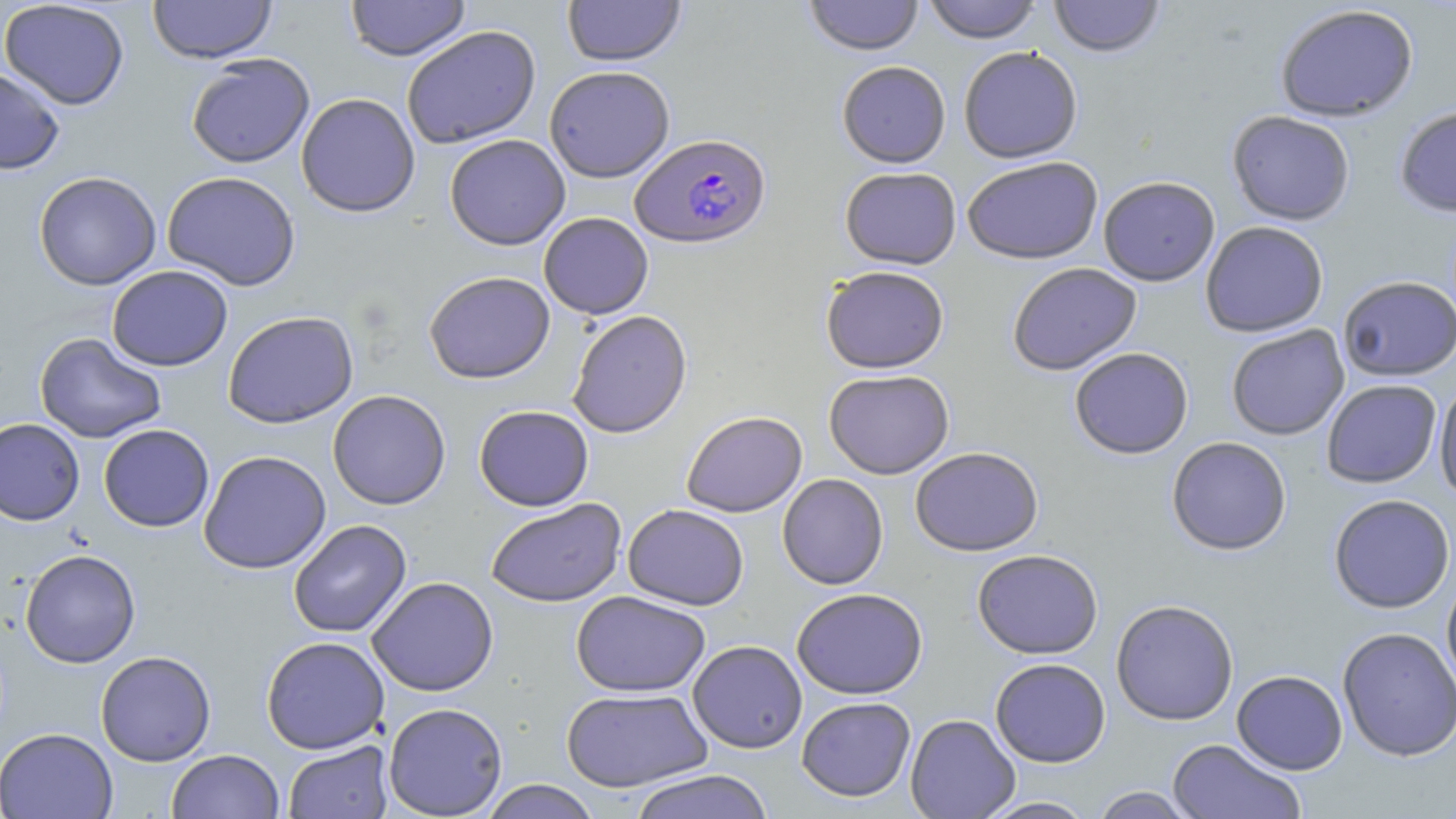

Summary:
  - Coordinate format: approximate bounding boxes as named x1/y1/x2/y2 corners in pixels
  - Uninfected red blood cell locations: (x1=148, y1=0, x2=277, y2=64), (x1=344, y1=0, x2=471, y2=61), (x1=562, y1=0, x2=687, y2=66), (x1=803, y1=0, x2=924, y2=56), (x1=923, y1=0, x2=1042, y2=44), (x1=1048, y1=0, x2=1166, y2=58), (x1=0, y1=1, x2=130, y2=110), (x1=1274, y1=5, x2=1419, y2=122), (x1=401, y1=25, x2=541, y2=149), (x1=958, y1=46, x2=1083, y2=164), (x1=185, y1=54, x2=314, y2=168), (x1=836, y1=61, x2=951, y2=168), (x1=544, y1=65, x2=675, y2=182), (x1=0, y1=67, x2=66, y2=175), (x1=296, y1=92, x2=420, y2=217), (x1=1394, y1=105, x2=1456, y2=218), (x1=1227, y1=111, x2=1355, y2=226), (x1=444, y1=134, x2=570, y2=250), (x1=962, y1=157, x2=1104, y2=265), (x1=840, y1=167, x2=962, y2=269), (x1=34, y1=171, x2=162, y2=290), (x1=162, y1=171, x2=301, y2=291), (x1=1098, y1=176, x2=1220, y2=287), (x1=539, y1=212, x2=653, y2=319), (x1=1200, y1=221, x2=1328, y2=338), (x1=1007, y1=263, x2=1142, y2=376), (x1=107, y1=265, x2=233, y2=371), (x1=820, y1=265, x2=950, y2=374), (x1=424, y1=271, x2=555, y2=384), (x1=1337, y1=275, x2=1455, y2=381), (x1=222, y1=310, x2=358, y2=428), (x1=568, y1=310, x2=692, y2=438), (x1=1226, y1=324, x2=1349, y2=441), (x1=34, y1=332, x2=167, y2=443), (x1=1069, y1=347, x2=1194, y2=460), (x1=823, y1=369, x2=954, y2=479), (x1=1322, y1=379, x2=1442, y2=488), (x1=1433, y1=379, x2=1456, y2=506), (x1=327, y1=389, x2=451, y2=510), (x1=474, y1=405, x2=594, y2=511), (x1=681, y1=411, x2=807, y2=517), (x1=0, y1=418, x2=84, y2=526), (x1=98, y1=424, x2=214, y2=532), (x1=1166, y1=437, x2=1291, y2=556), (x1=910, y1=447, x2=1044, y2=557), (x1=198, y1=450, x2=331, y2=574), (x1=777, y1=474, x2=889, y2=590), (x1=1328, y1=494, x2=1455, y2=614), (x1=486, y1=498, x2=627, y2=607), (x1=623, y1=504, x2=749, y2=610), (x1=288, y1=520, x2=412, y2=638), (x1=19, y1=549, x2=141, y2=668), (x1=972, y1=549, x2=1103, y2=660), (x1=1441, y1=574, x2=1456, y2=695), (x1=367, y1=577, x2=499, y2=696), (x1=791, y1=587, x2=928, y2=699), (x1=571, y1=591, x2=710, y2=697), (x1=1111, y1=600, x2=1238, y2=726), (x1=1337, y1=627, x2=1456, y2=762), (x1=261, y1=636, x2=390, y2=754), (x1=688, y1=640, x2=807, y2=753), (x1=96, y1=650, x2=216, y2=765), (x1=990, y1=658, x2=1111, y2=768), (x1=1231, y1=670, x2=1348, y2=775), (x1=561, y1=687, x2=713, y2=792), (x1=796, y1=696, x2=916, y2=802), (x1=383, y1=702, x2=508, y2=818), (x1=905, y1=714, x2=1020, y2=818), (x1=0, y1=727, x2=118, y2=819), (x1=1167, y1=739, x2=1305, y2=819), (x1=283, y1=741, x2=393, y2=818), (x1=166, y1=749, x2=284, y2=819), (x1=626, y1=769, x2=776, y2=819), (x1=478, y1=780, x2=602, y2=819), (x1=1090, y1=786, x2=1198, y2=818), (x1=976, y1=796, x2=1098, y2=818)
  - Plasmodium falciparum-infected red blood cell locations: (x1=630, y1=133, x2=770, y2=249)
  - Slide-level diagnosis: Plasmodium falciparum
  - Field of view: one of a larger specimen
  - Stain: May-Grünwald-Giemsa
  - Magnification: 1000x
  - Modality: light microscopy
  - Image size: 1456×819 pixels
  - Preparation: thin blood film